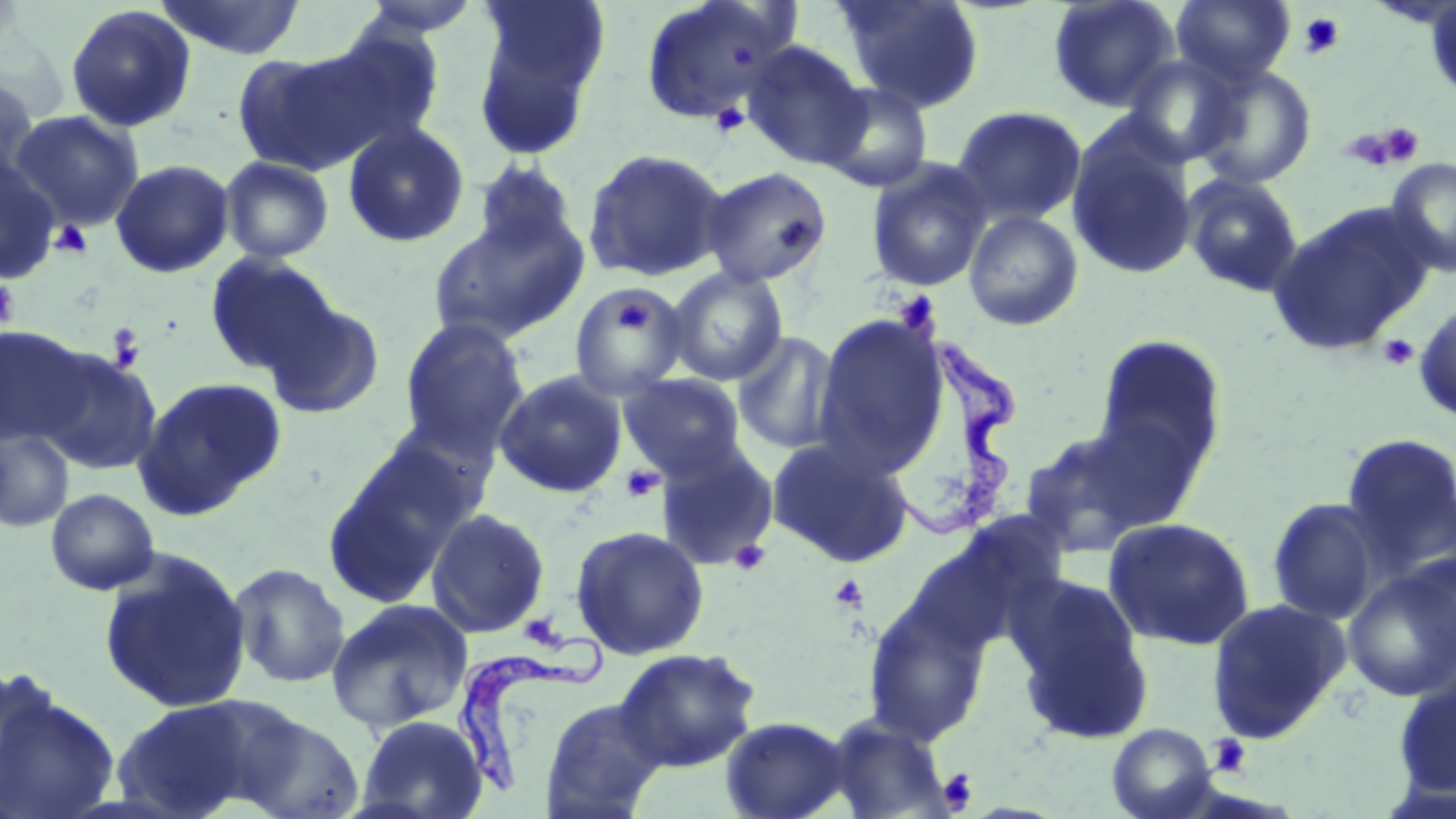 Approximate bounding boxes as (x1,y1)-(x2,y2) corner pairs in pixels. Trypanosoma brucei locations: (886,336)-(1021,545), (453,629)-(606,794). Uninfected red blood cell locations: (155,0)-(307,60), (354,0)-(485,37), (639,0)-(800,128), (837,0)-(985,113), (1047,0)-(1181,113), (1171,0)-(1296,87), (1424,1)-(1456,103), (471,2)-(610,159), (65,4)-(197,132), (312,24)-(446,151), (741,41)-(871,171), (234,45)-(387,175), (1121,55)-(1245,167), (1192,63)-(1318,189), (0,75)-(40,189), (819,81)-(934,193), (952,106)-(1087,227), (8,110)-(144,231), (342,122)-(470,248), (1066,125)-(1198,280), (581,147)-(731,283), (0,156)-(61,284), (219,156)-(335,263), (1386,157)-(1456,278), (470,158)-(581,261), (865,158)-(992,293), (110,159)-(234,278), (700,166)-(833,288), (1181,172)-(1305,297), (1270,203)-(1435,355), (963,209)-(1085,331), (427,213)-(589,345), (204,252)-(340,378), (665,266)-(789,386), (568,281)-(690,400), (261,295)-(386,421), (1414,302)-(1456,423), (811,312)-(950,480), (399,317)-(529,455), (0,324)-(91,447), (732,331)-(844,455), (1093,334)-(1228,482), (33,347)-(162,475), (494,370)-(628,498), (619,373)-(747,483), (135,377)-(286,516), (1018,424)-(1166,558), (1,428)-(74,533), (1339,432)-(1456,578), (766,437)-(914,568), (654,439)-(780,569), (323,440)-(471,607), (45,488)-(160,595), (1266,497)-(1386,625), (425,507)-(550,638), (1103,516)-(1257,651), (570,524)-(710,661), (99,553)-(252,713), (1342,561)-(1456,703), (229,563)-(350,689), (1006,573)-(1154,745), (862,593)-(992,747), (326,597)-(474,734), (1206,598)-(1351,743), (612,647)-(761,772), (1391,671)-(1456,800), (0,683)-(120,819), (112,697)-(264,817), (538,698)-(666,819), (228,708)-(365,818), (356,714)-(487,819), (822,714)-(953,818), (719,716)-(853,819), (1106,723)-(1218,819). Platelet locations: (1297,11)-(1346,59), (709,102)-(750,139), (1343,124)-(1422,171), (49,220)-(94,258), (0,278)-(20,329), (894,292)-(939,330), (616,294)-(649,332), (107,323)-(146,374), (1377,333)-(1420,371), (620,465)-(664,502), (729,540)-(771,577), (829,573)-(870,613), (518,613)-(566,650), (1208,734)-(1252,777), (938,768)-(978,812). Slide-level diagnosis: Trypanosoma brucei. Image is 1456×819 pixels. Single field of view. May-Grünwald-Giemsa-stained preparation. 1000x magnification. Thin blood film. Optical microscopy.